Locate leukocytes (white blood cells).
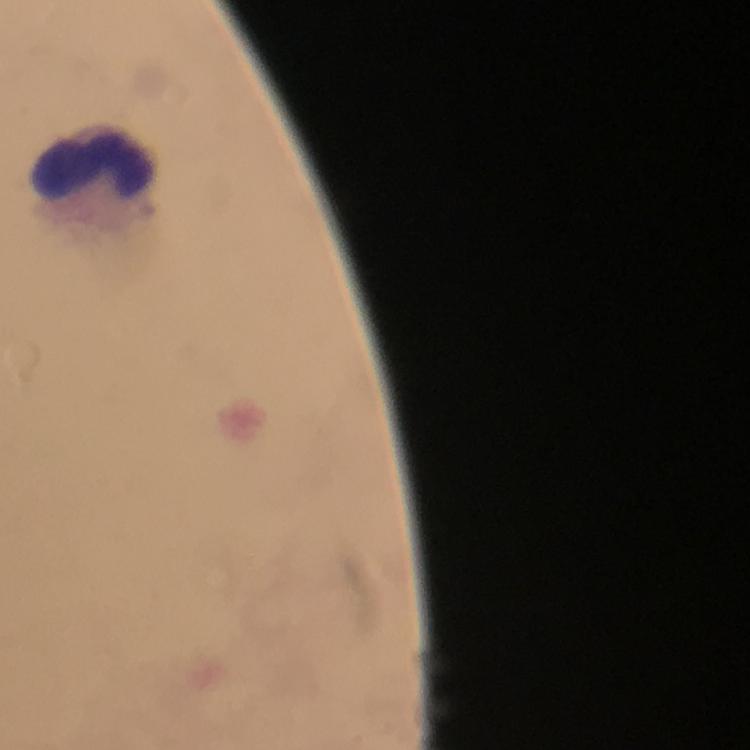
Approximate object centers, in pixels from the top-left corner.
Leukocytes: (x=94, y=159).

Summary:
  - Context: from a diagnostic examination for malaria
  - Cropped from: one field of view
  - Image size: 750×750 pixels
  - Malaria parasites: none detected
  - Immersion oil: applied
  - Stain: Giemsa
  - Preparation: thick blood film
  - Capture: smartphone camera through the microscope
  - Magnification: 100x